Give the position of every malaria parasite.
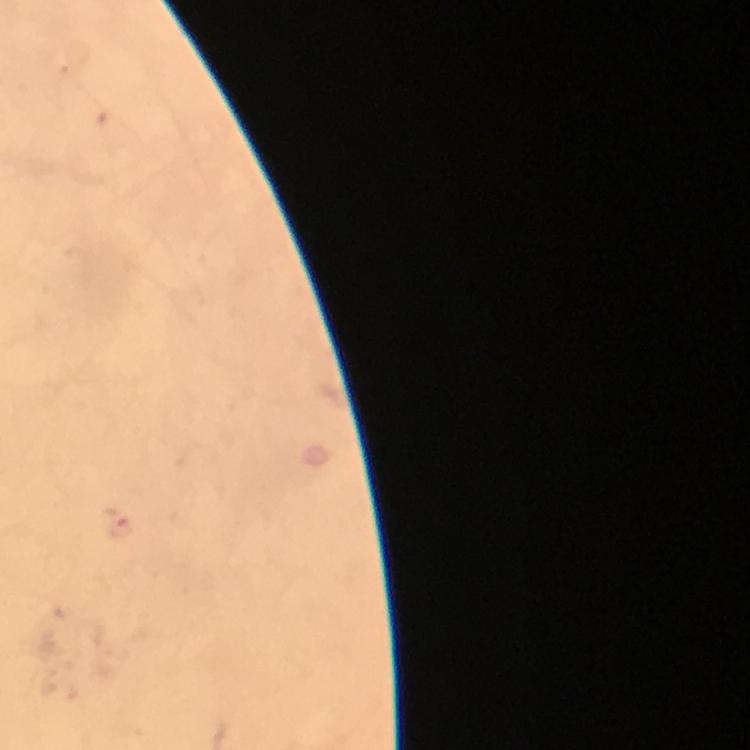
Approximate centers as {x, y} in pixels.
Malaria parasites: {121, 525}.

Summary:
  - Magnification: 100x
  - Cropped from: a single field of view
  - Image size: 750×750 pixels
  - Stain: Giemsa
  - Context: from a diagnostic examination for malaria
  - Preparation: thick smear
  - Capture: smartphone photograph through a microscope
  - Immersion oil: applied